Comment on the morphology of the erythrocytes.
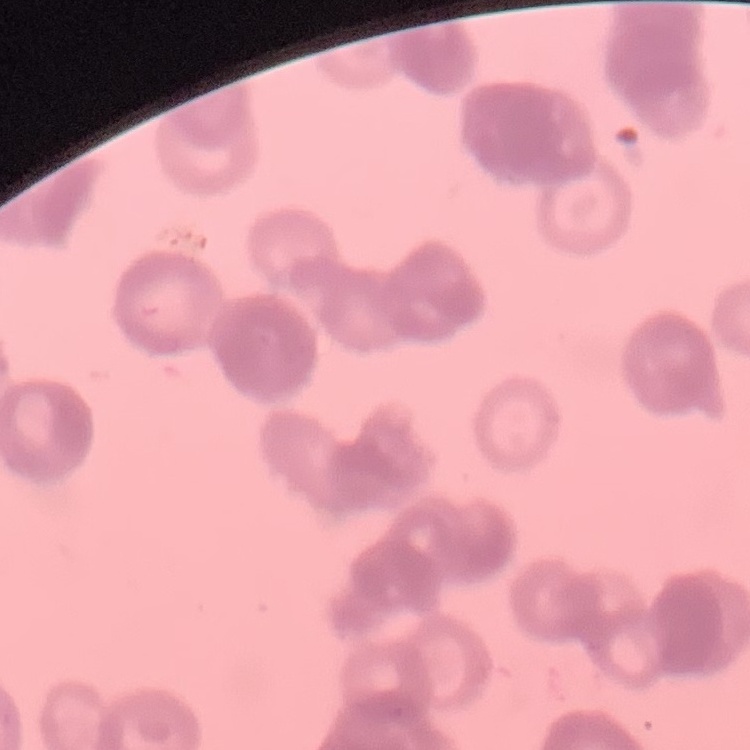

They show rouleaux formation.

Summary:
  - Image type: square crop of a larger photomicrograph
  - Stain: Field's or Giemsa
  - Preparation: thin blood smear